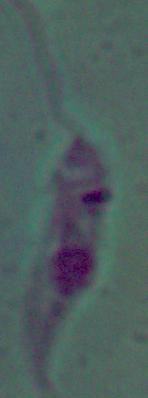
magnification = 1000x
modality = photomicrograph
identification = Leishmania